Assess this cell for malaria.
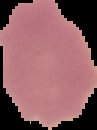

Uninfected.

Cell region segmented out of the field of view; the surrounding area is masked to black. Image is 97×130 pixels. From a thin blood film.